Give the preparation type.
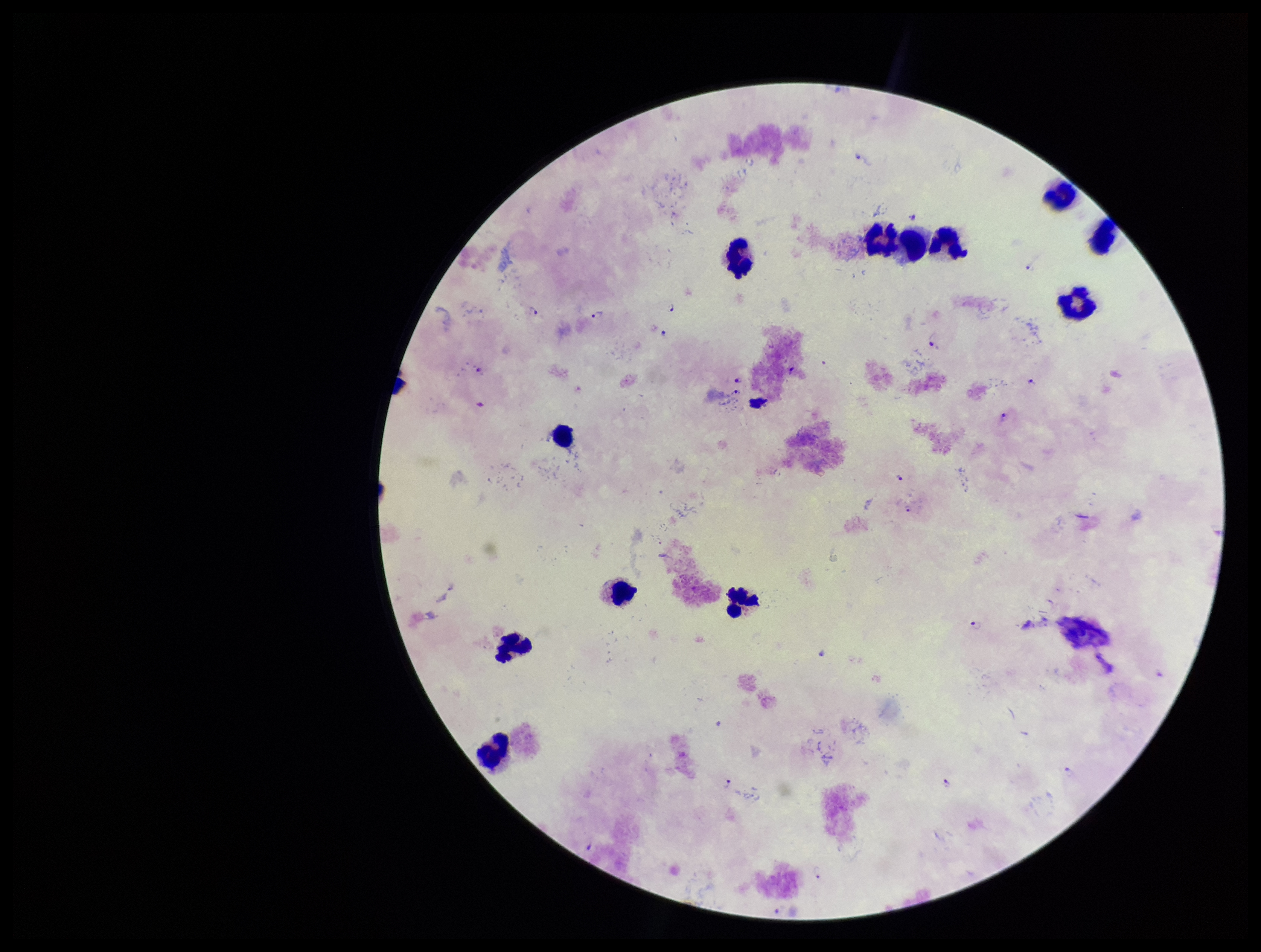
It is a thick blood smear.

Summary:
  - Image size: 1261×952 pixels
  - Stain: Giemsa
  - Parasite count: 16
  - Field of view: single
  - Leukocyte count: 12
  - Capture: smartphone photograph through the microscope eyepiece
  - Plasmodium parasites: seen
  - Species reported for this patient: Plasmodium falciparum
  - Patient malaria status: positive